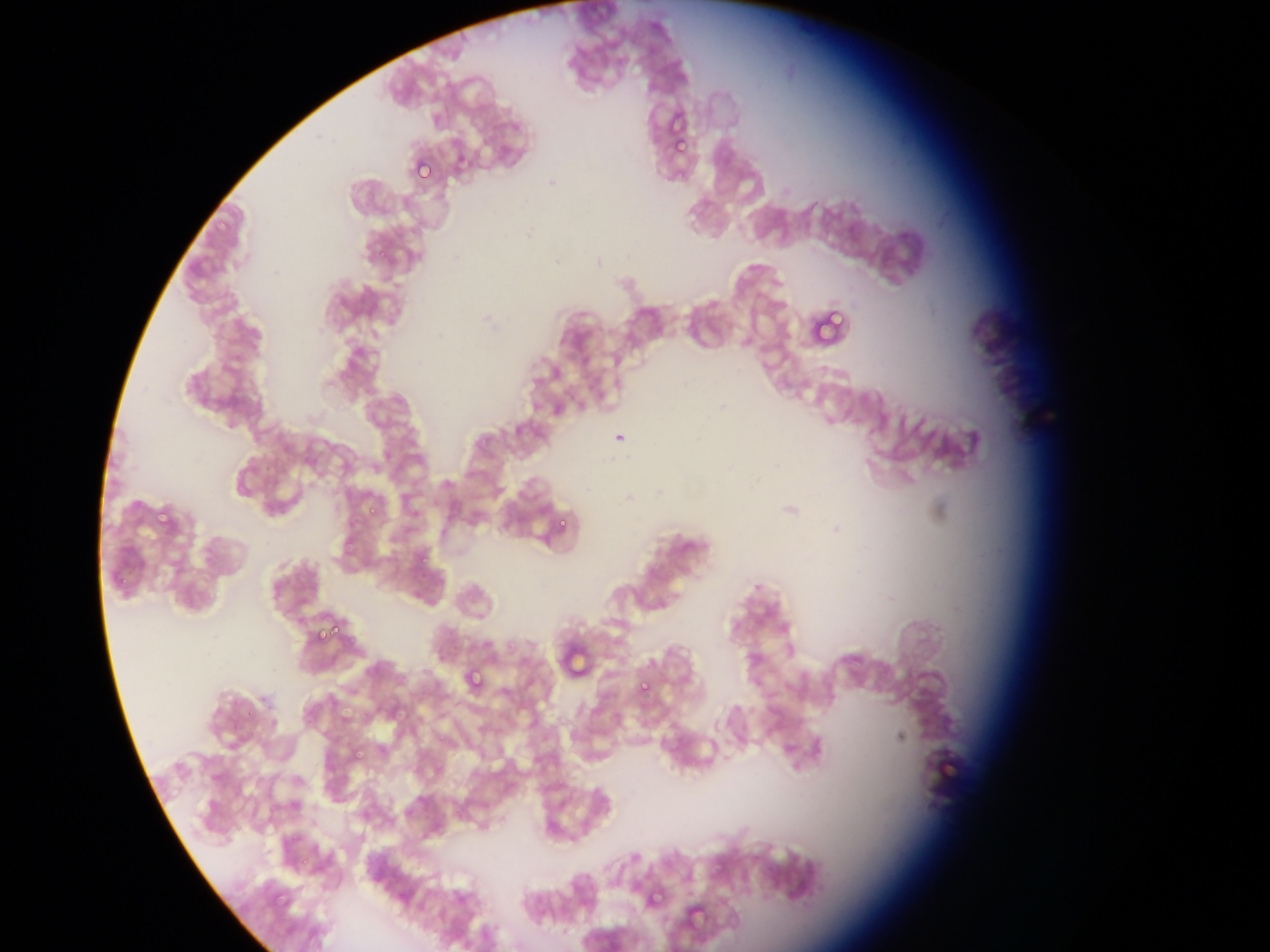

Approximate bounding boxes as left top right bottom in pixels. Plasmodium parasite locations: 674 130 693 152; 414 160 433 180; 830 309 844 327; 613 424 632 446; 365 500 384 515; 154 509 168 523; 553 519 570 530; 312 612 326 647; 330 625 340 639; 462 668 484 689; 637 671 659 698. Image is 1270×952 pixels. Sample from Ghana. Photographed through a microscope with a mobile-phone camera. One field of view. Thin blood smear.